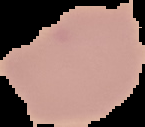
result = negative for Plasmodium parasites
preparation = thin blood film
image type = segmented cell region on a black background
image size = 145×127 pixels